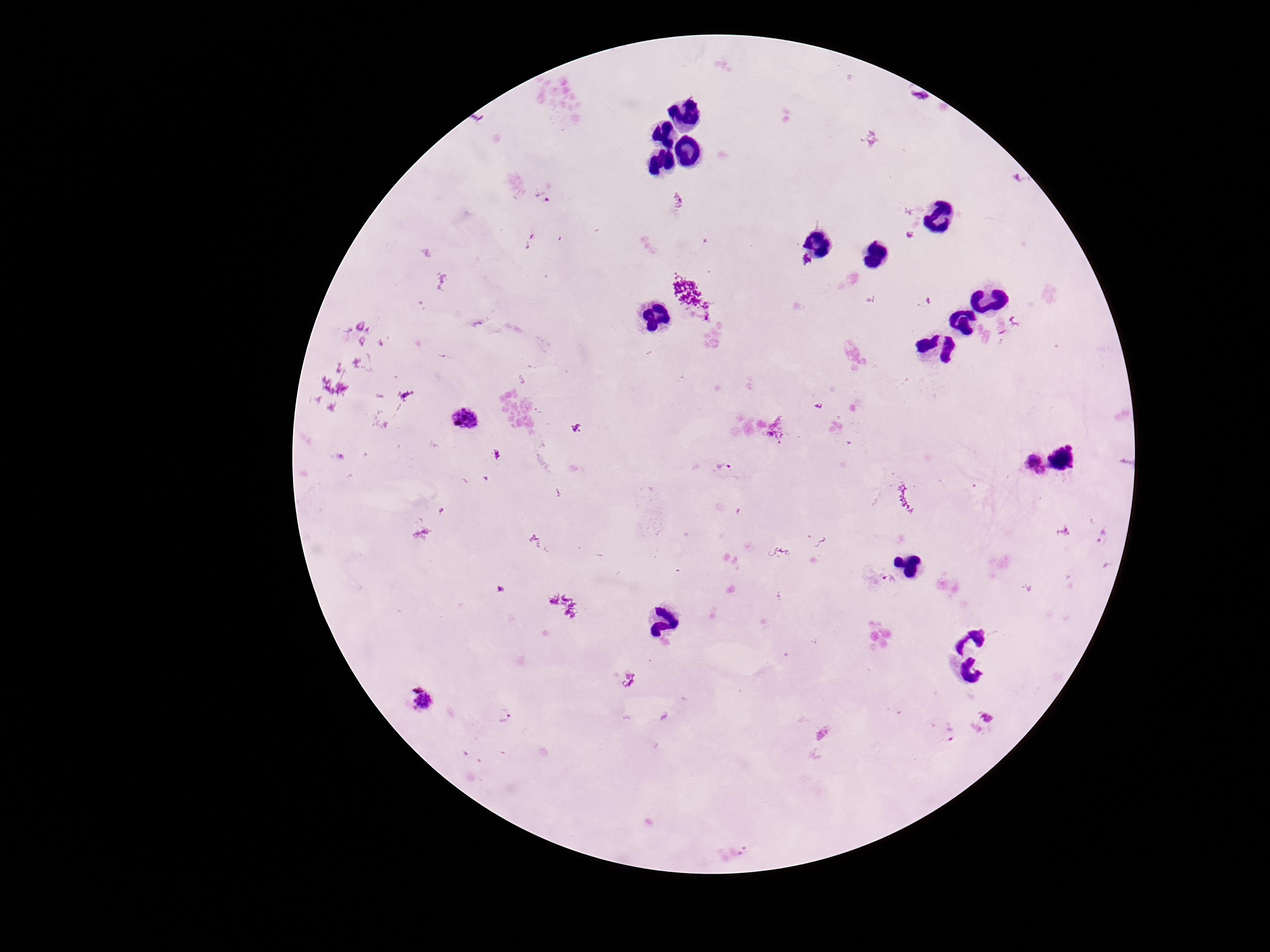

Approximate object centers, in pixels from the top-left corner.
Summary:
  - Plasmodium parasite locations: (x=543, y=196), (x=693, y=295), (x=476, y=324), (x=465, y=420), (x=578, y=428), (x=1069, y=458), (x=724, y=468), (x=1028, y=468), (x=890, y=581), (x=422, y=701), (x=504, y=713), (x=951, y=733)
  - Preparation: thick blood smear
  - Patient malaria status: positive
  - Magnification: 100x
  - Capture: smartphone camera through the microscope eyepiece
  - Field of view: one from this slide
  - Stain: Giemsa
  - Image size: 1270×952 pixels